Identify the parasite.
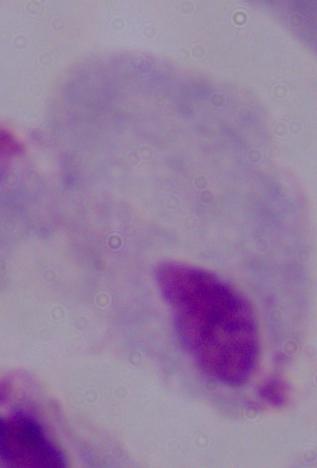

This is a trichomonad.

Summary:
  - Modality: photomicrograph
  - Magnification: 1000x